Name the blood parasite species.
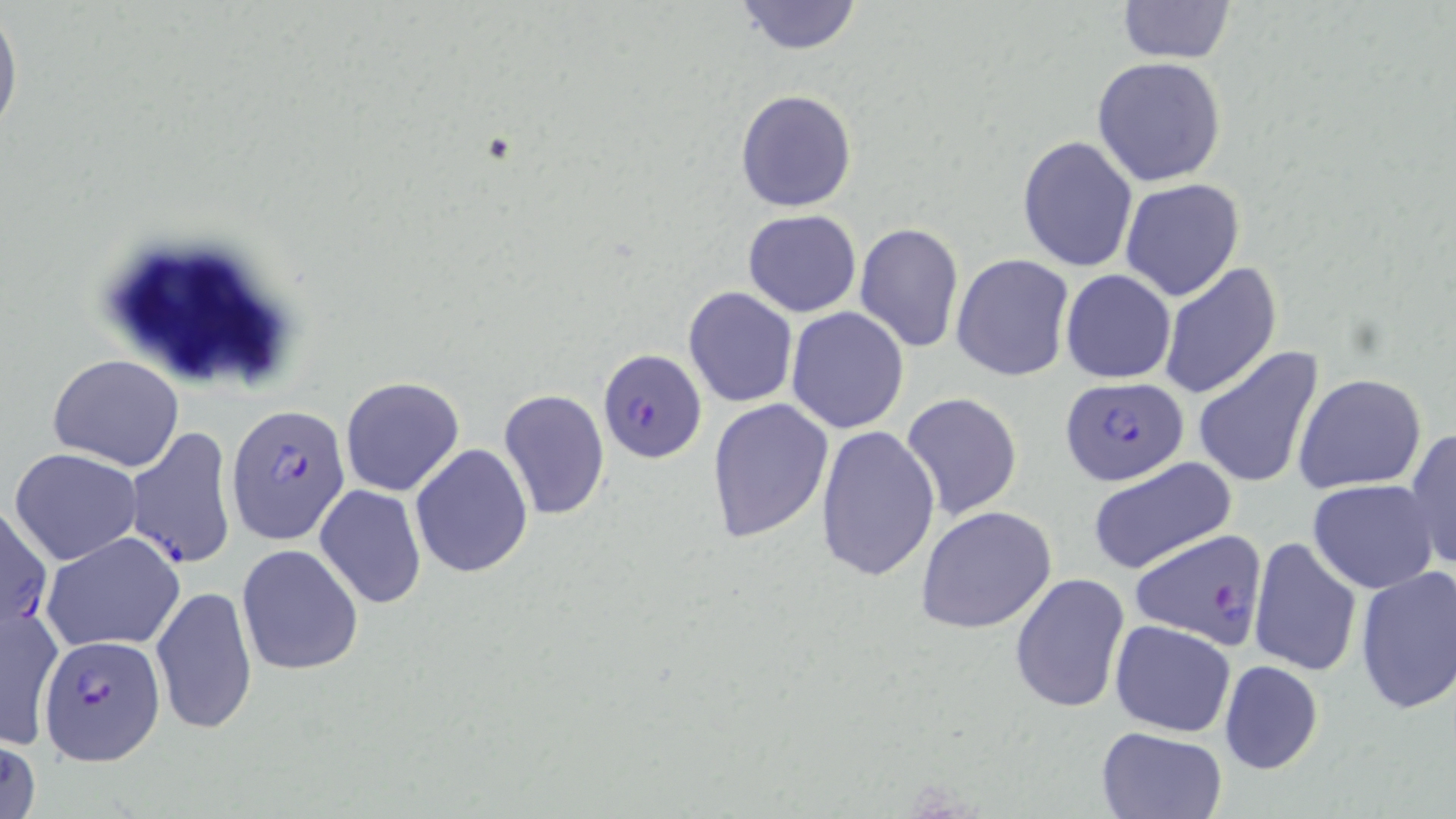

Plasmodium falciparum.

Approximate bounding boxes as named x1/y1/x2/y2 corners in pixels. Plasmodium falciparum-infected red blood cell locations: (x1=597, y1=345, x2=706, y2=462), (x1=1061, y1=377, x2=1188, y2=486), (x1=224, y1=402, x2=352, y2=547), (x1=124, y1=426, x2=238, y2=571), (x1=0, y1=506, x2=54, y2=635), (x1=1129, y1=527, x2=1268, y2=650), (x1=38, y1=632, x2=166, y2=764). Uninfected red blood cell locations: (x1=735, y1=1, x2=862, y2=54), (x1=1114, y1=1, x2=1237, y2=64), (x1=0, y1=6, x2=22, y2=144), (x1=1092, y1=57, x2=1227, y2=188), (x1=735, y1=88, x2=857, y2=212), (x1=1017, y1=135, x2=1140, y2=272), (x1=1119, y1=178, x2=1246, y2=301), (x1=743, y1=209, x2=861, y2=317), (x1=853, y1=221, x2=964, y2=354), (x1=952, y1=253, x2=1074, y2=380), (x1=1158, y1=261, x2=1282, y2=399), (x1=1060, y1=268, x2=1177, y2=384), (x1=683, y1=287, x2=798, y2=407), (x1=785, y1=306, x2=910, y2=432), (x1=1191, y1=344, x2=1326, y2=492), (x1=46, y1=354, x2=187, y2=473), (x1=1293, y1=374, x2=1426, y2=495), (x1=340, y1=376, x2=466, y2=497), (x1=499, y1=389, x2=610, y2=522), (x1=900, y1=392, x2=1022, y2=521), (x1=706, y1=399, x2=833, y2=545), (x1=815, y1=424, x2=941, y2=583), (x1=1405, y1=427, x2=1456, y2=575), (x1=409, y1=443, x2=533, y2=579), (x1=9, y1=447, x2=143, y2=565), (x1=1086, y1=455, x2=1238, y2=576), (x1=1308, y1=479, x2=1438, y2=594), (x1=315, y1=485, x2=427, y2=609), (x1=914, y1=505, x2=1058, y2=634), (x1=41, y1=531, x2=186, y2=653), (x1=1248, y1=537, x2=1363, y2=678), (x1=236, y1=543, x2=364, y2=675), (x1=1354, y1=564, x2=1456, y2=715), (x1=1009, y1=572, x2=1131, y2=714), (x1=151, y1=583, x2=258, y2=735), (x1=2, y1=601, x2=63, y2=752), (x1=1109, y1=619, x2=1236, y2=736), (x1=1217, y1=659, x2=1324, y2=776), (x1=1094, y1=726, x2=1228, y2=819), (x1=1, y1=735, x2=43, y2=819). Thin blood smear. One field of a larger specimen. Image is 1456×819 pixels. Captured at 1000x magnification. May-Grünwald-Giemsa-stained preparation. Light microscopy.